Give the position of every Plasmodium parasite.
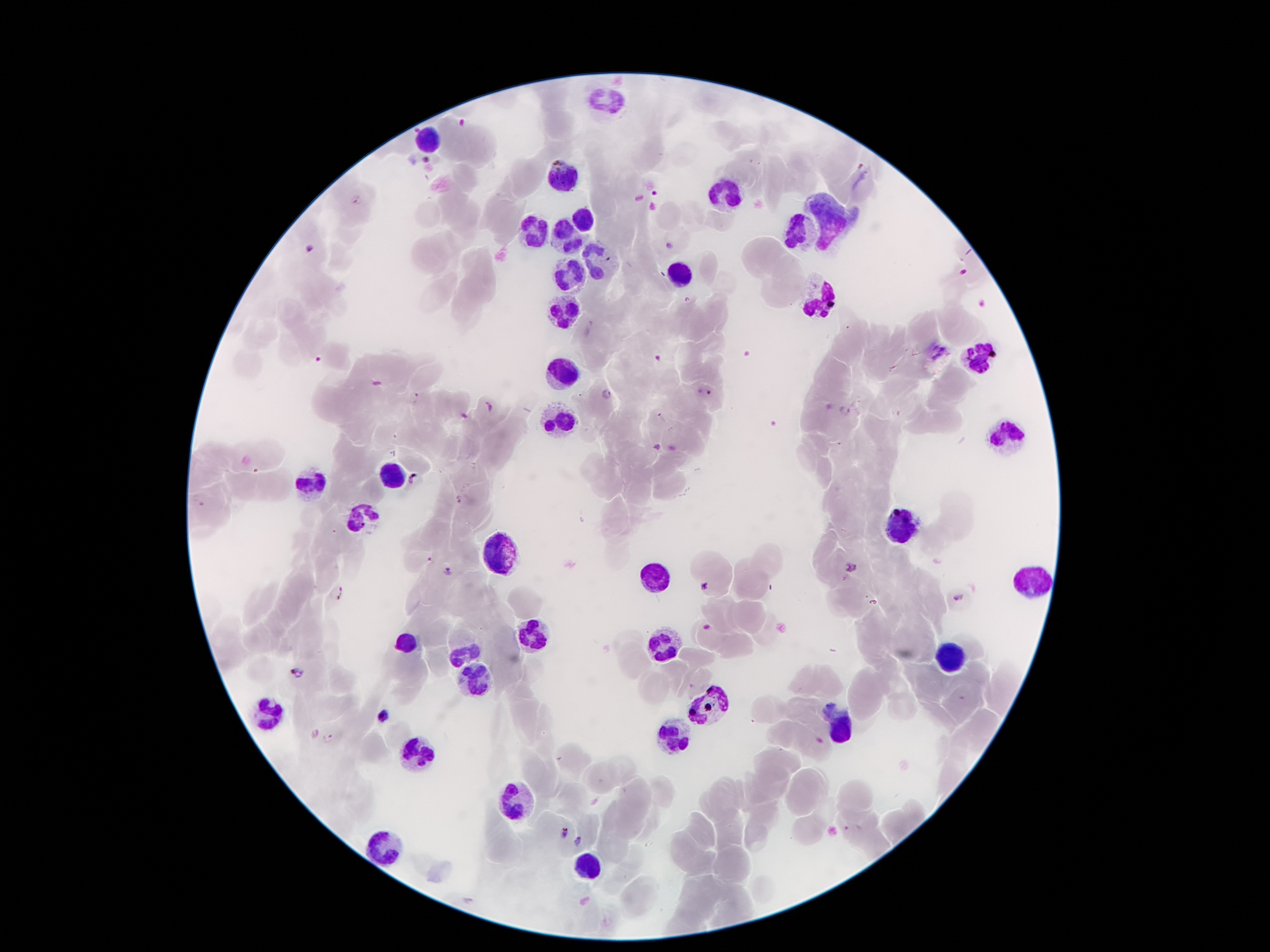

Approximate centers as (x, y) in pixels.
Plasmodium parasites: (655, 195), (356, 201), (669, 247), (309, 250), (317, 358), (657, 359), (703, 392), (606, 394), (416, 396), (489, 408), (846, 409), (662, 418), (655, 447), (413, 478), (458, 500), (429, 559), (852, 568), (448, 570), (706, 585), (336, 593), (958, 599), (705, 626), (298, 673), (385, 714), (330, 739), (564, 832), (578, 840).

Leukocyte locations: (607, 101), (425, 143), (561, 177), (721, 199), (579, 221), (829, 223), (801, 227), (531, 231), (565, 237), (595, 257), (573, 273), (677, 277), (821, 297), (567, 309), (977, 352), (565, 374), (563, 420), (1013, 430), (391, 470), (311, 482), (359, 512), (899, 528), (499, 554), (653, 580), (1031, 580), (529, 634), (405, 644), (661, 644), (463, 652), (951, 652), (477, 682), (713, 700), (263, 712), (839, 724), (673, 738), (417, 754), (521, 798), (383, 842), (589, 870). 100x magnification. Single field of view. Patient malaria status: infected with Plasmodium falciparum. Photographed through the microscope eyepiece with a smartphone camera. Image is 1270×952 pixels. Thick blood smear. Giemsa stain.